Report the malaria status of this cell.
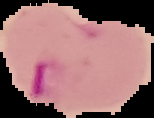

It is parasitized.

Summary:
  - Preparation: thin blood film
  - Image type: segmented cell region with the area outside set to black
  - Image size: 154×118 pixels